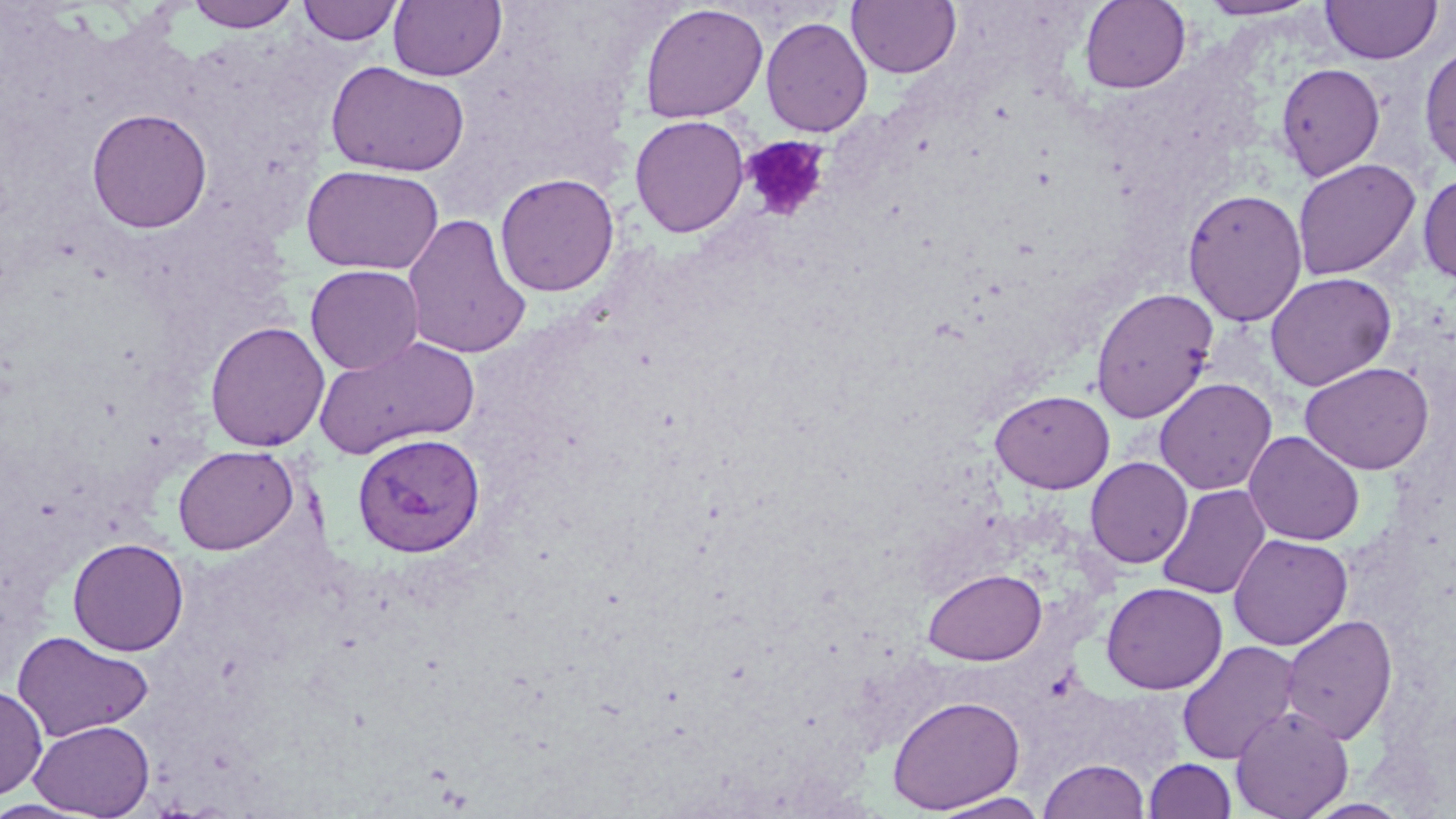
Summary:
  - Coordinate format: approximate bounding boxes as (x1,y1)-(x2,y2) corner pairs in pixels
  - Platelet locations: (741,134)-(830,222)
  - Uninfected red blood cell locations: (186,0)-(300,31), (1079,0)-(1191,94), (1196,0)-(1322,21), (1321,0)-(1442,64), (297,1)-(403,45), (388,1)-(507,82), (847,1)-(961,79), (639,3)-(768,123), (760,16)-(873,137), (1419,43)-(1456,176), (326,60)-(471,177), (1276,63)-(1385,181), (86,108)-(213,233), (629,115)-(749,237), (1292,158)-(1421,280), (301,164)-(444,275), (495,172)-(621,297), (1418,172)-(1456,286), (1182,188)-(1308,327), (402,213)-(532,360), (305,264)-(424,375), (1265,272)-(1397,391), (1090,287)-(1219,423), (204,321)-(330,452), (314,335)-(479,457), (1299,361)-(1435,475), (1154,377)-(1277,495), (989,389)-(1115,494), (1244,430)-(1365,546), (172,445)-(298,555), (1085,457)-(1193,569), (1157,484)-(1270,600), (1229,534)-(1352,650), (67,537)-(189,656), (923,568)-(1047,665), (1101,581)-(1228,695), (1280,615)-(1399,744), (12,631)-(155,742), (1176,640)-(1302,765), (0,684)-(48,801), (887,694)-(1025,814), (1230,705)-(1353,819), (29,720)-(155,818), (1038,758)-(1151,819), (1143,758)-(1237,818), (929,792)-(1050,818), (1300,798)-(1414,818)
  - Plasmodium vivax-infected red blood cell locations: (352,433)-(485,557)
  - Slide-level diagnosis: Plasmodium vivax
  - Modality: optical microscopy
  - Field of view: one of a larger specimen
  - Stain: May-Grünwald-Giemsa
  - Preparation: thin blood smear
  - Image size: 1456×819 pixels
  - Magnification: 1000x